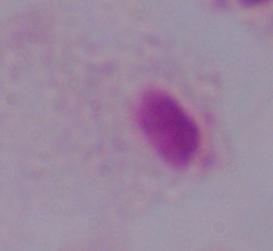

1000x magnification. A trichomonad is seen. Micrograph.